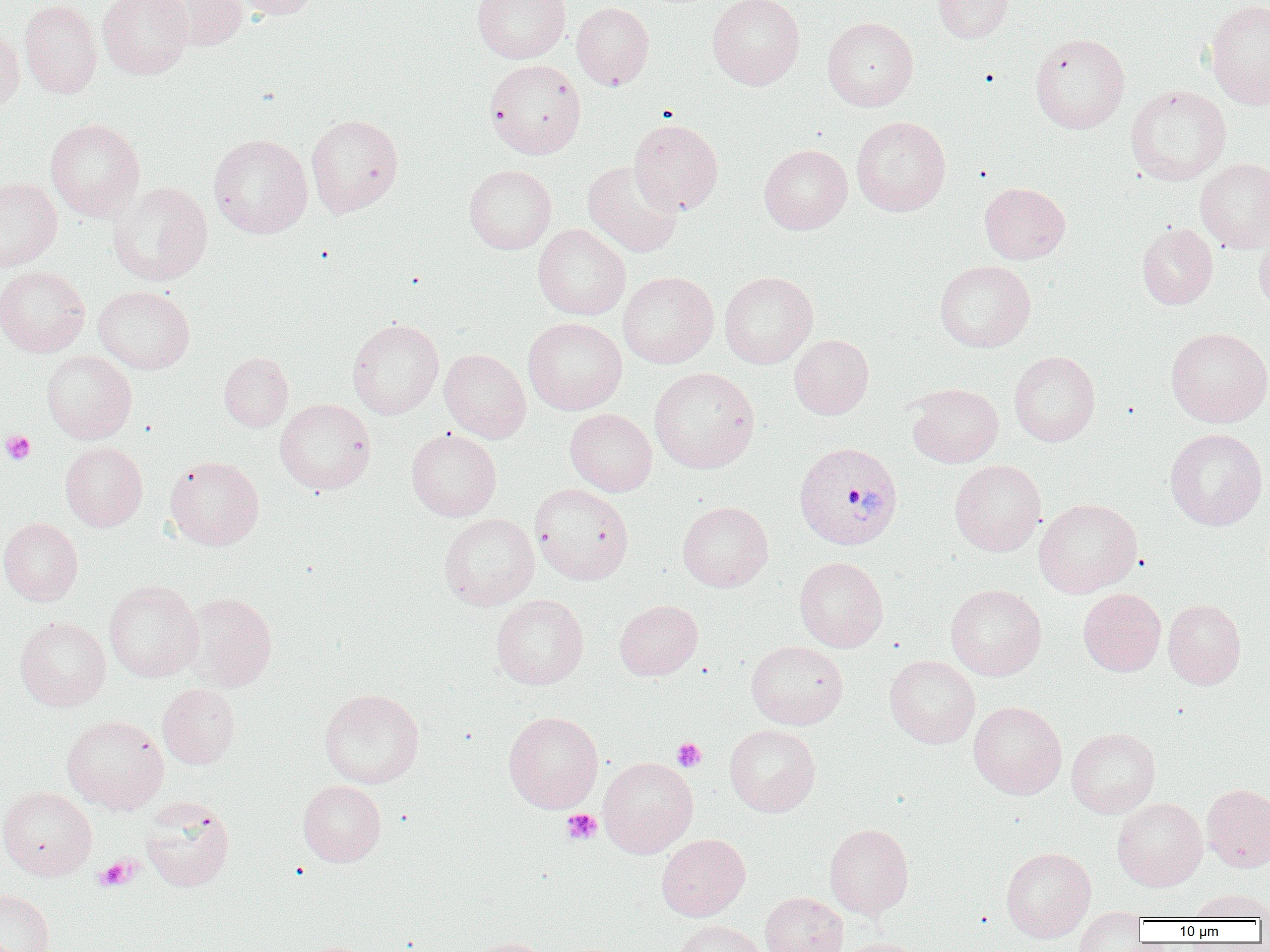
{
  "slide_level_diagnosis": "Plasmodium vivax",
  "magnification": "1000x",
  "image_size": "1270×952 pixels",
  "preparation": "thin blood smear",
  "field_of_view": "single",
  "uninfected_red_blood_cell_locations": "approximate bounding boxes as [x1, y1, x2, y2] in pixels: [19, 0, 102, 99], [98, 0, 192, 80], [150, 0, 248, 51], [233, 0, 320, 20], [707, 0, 805, 90], [933, 0, 1013, 44], [472, 1, 571, 63], [1205, 1, 1270, 110], [572, 2, 654, 90], [822, 16, 918, 111], [0, 28, 24, 117], [1030, 32, 1130, 134], [485, 59, 586, 158], [1125, 85, 1231, 185], [306, 114, 403, 217], [852, 115, 950, 216], [45, 118, 145, 221], [629, 118, 723, 215], [209, 134, 313, 238], [759, 144, 852, 234], [1195, 158, 1270, 253], [583, 160, 683, 257], [464, 164, 556, 254], [0, 178, 62, 272], [108, 182, 213, 286], [979, 182, 1070, 264], [1137, 223, 1218, 309], [533, 224, 631, 320], [1254, 234, 1270, 315], [934, 260, 1035, 353], [0, 266, 90, 357], [618, 271, 719, 368], [719, 271, 818, 369], [93, 285, 195, 374], [522, 317, 627, 415], [347, 318, 443, 419], [1166, 327, 1270, 427], [789, 334, 874, 419], [439, 348, 531, 443], [41, 350, 136, 444], [1009, 350, 1100, 446], [219, 352, 293, 431], [649, 367, 760, 473], [906, 383, 1004, 468], [275, 398, 375, 494], [565, 408, 657, 496], [406, 428, 502, 521], [1165, 428, 1268, 531], [60, 442, 147, 531], [165, 456, 264, 550], [949, 459, 1046, 556], [531, 483, 633, 585], [1034, 498, 1143, 597], [677, 501, 773, 592], [439, 513, 539, 610], [0, 517, 83, 605], [794, 557, 888, 652], [104, 580, 203, 682], [946, 584, 1046, 680], [1078, 588, 1166, 676], [181, 592, 277, 692], [491, 594, 588, 689], [1163, 599, 1246, 689], [615, 600, 702, 680], [14, 616, 111, 711], [746, 640, 848, 729], [884, 655, 980, 748], [158, 683, 240, 768], [319, 688, 424, 788], [968, 701, 1067, 799], [503, 711, 603, 813], [61, 715, 168, 813], [724, 724, 820, 816], [1066, 727, 1160, 818], [598, 756, 698, 858], [298, 780, 386, 867], [1202, 784, 1270, 871], [0, 787, 96, 880], [141, 796, 235, 891], [1112, 797, 1207, 891], [825, 823, 914, 919], [656, 834, 750, 921], [1000, 846, 1096, 942], [0, 888, 55, 952], [1189, 888, 1270, 921], [760, 891, 848, 952], [1073, 908, 1146, 951], [672, 920, 768, 952], [465, 937, 555, 952], [836, 937, 927, 952]",
  "plasmodium_vivax_infected_red_blood_cell_locations": "approximate bounding boxes as [x1, y1, x2, y2] in pixels: [793, 441, 904, 550]",
  "platelet_locations": "approximate bounding boxes as [x1, y1, x2, y2] in pixels: [1, 429, 36, 465], [672, 737, 706, 771], [562, 808, 601, 845], [95, 856, 138, 891]",
  "modality": "optical microscopy"
}